Classify this cell by malaria status.
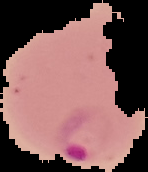
Parasitized.

image_type: cell region segmented out of the field of view; surrounding area masked to black
preparation: thin blood film
image_size: 148×172 pixels